Assess this cell for malaria.
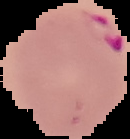

Parasitized.

Summary:
  - Image size: 130×139 pixels
  - Image type: segmented cell region with the area outside set to black
  - Preparation: thin blood film